Identify the parasite.
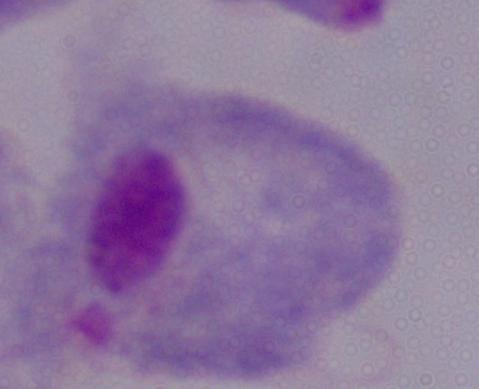

A trichomonad.

Summary:
  - Magnification: 1000x
  - Modality: photomicrograph